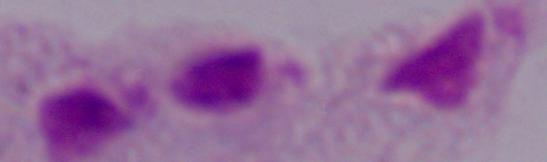
Summary:
  - Modality: photomicrograph
  - Identification: trichomonad
  - Magnification: 1000x